Point out each Plasmodium parasite.
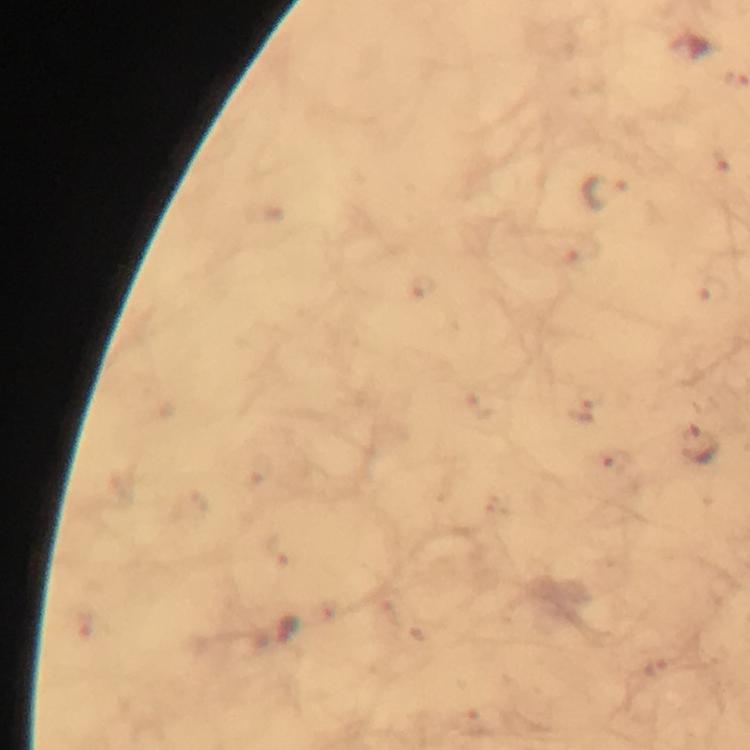

Approximate centers as (x, y) in pixels.
Plasmodium parasites: (605, 193), (589, 397), (701, 444), (615, 462).

Summary:
  - Immersion oil: used
  - Context: from a diagnostic examination for malaria
  - Cropped from: one field of view
  - Preparation: thick blood smear
  - Stain: Giemsa
  - Magnification: 100x
  - Capture: smartphone camera through the microscope
  - Image size: 750×750 pixels